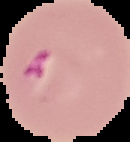
preparation = thin blood film
image size = 130×142 pixels
image type = segmented cell region with the area outside set to black
malaria status = parasitized